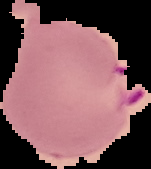
Summary:
  - Malaria status: parasitized
  - Image size: 151×169 pixels
  - Image type: segmented cell region with the area outside set to black
  - Preparation: thin blood film